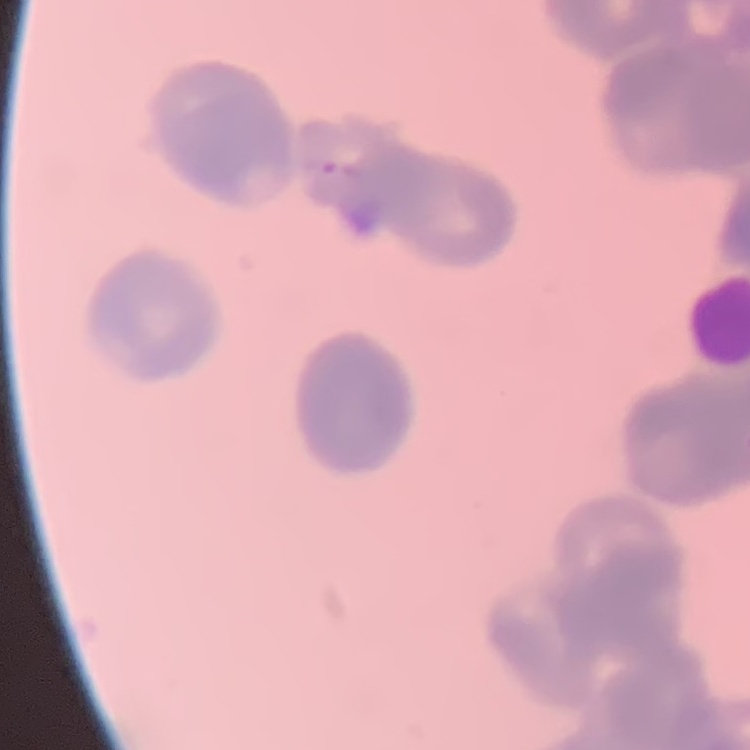
red blood cell morphology = rouleaux formation
image type = one tile cut from a larger photomicrograph
preparation = thin blood smear
stain = Field's or Giemsa